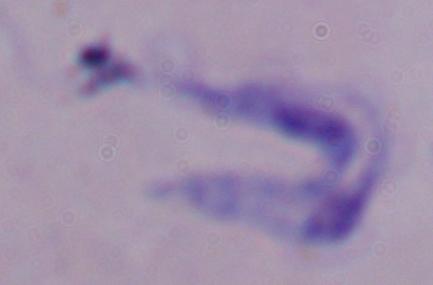
{
  "identification": "trypanosome",
  "modality": "micrograph",
  "magnification": "1000x"
}